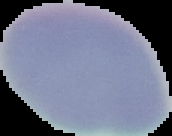

Malaria status: uninfected. Image is 172×136 pixels. Cell region segmented out of the field of view; the surrounding area is masked to black. From a thin blood smear.